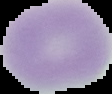
From a thin blood film. Malaria status: uninfected. Image is 112×94 pixels. The area outside the segmented cell region is set to black.